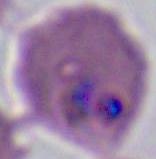
{
  "identification": "Plasmodium",
  "magnification": "400x or 1000x",
  "modality": "photomicrograph"
}